Report the malaria status of this cell.
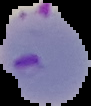

It is parasitized.

The area outside the segmented cell region is set to black. From a thin blood smear. Image is 91×106 pixels.